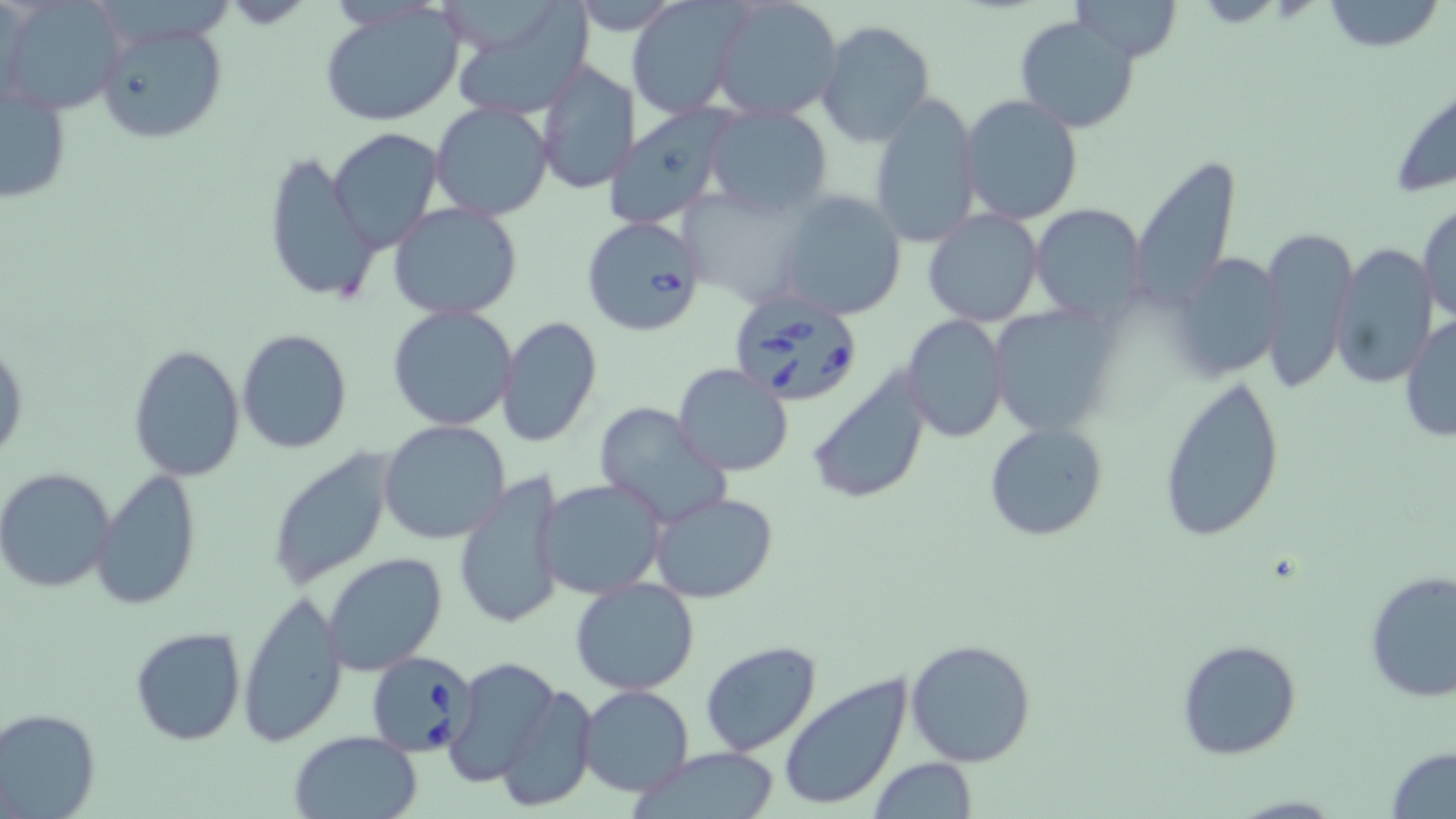

slide-level diagnosis = Babesia divergens
preparation = thin blood film
stain = May-Grünwald-Giemsa
image size = 1456×819 pixels
field of view = one of a larger specimen
magnification = 1000x
Babesia divergens-infected red blood cell locations = approximate bounding boxes as (x1, y1, x2, y2) in pixels: (580, 215, 709, 339), (729, 291, 863, 408), (367, 651, 480, 757)
modality = optical microscopy
uninfected red blood cell locations = approximate bounding boxes as (x1, y1, x2, y2) in pixels: (2, 0, 125, 116), (626, 0, 743, 120), (710, 0, 845, 122), (1071, 0, 1181, 62), (1320, 0, 1442, 52), (446, 2, 595, 120), (318, 4, 465, 127), (1015, 14, 1142, 132), (95, 17, 230, 148), (816, 20, 936, 146), (535, 61, 639, 196), (1, 74, 73, 207), (1385, 79, 1456, 199), (867, 94, 981, 248), (957, 94, 1084, 227), (430, 101, 555, 221), (605, 104, 733, 229), (703, 105, 834, 218), (327, 128, 444, 255), (263, 149, 376, 305), (1126, 155, 1244, 315), (777, 190, 907, 317), (1416, 200, 1455, 329), (390, 201, 523, 319), (1029, 203, 1147, 324), (923, 208, 1043, 327), (1254, 223, 1358, 396), (1330, 243, 1438, 390), (1168, 253, 1286, 380), (982, 303, 1119, 437), (387, 304, 518, 431), (903, 315, 1008, 442), (1399, 315, 1456, 443), (496, 317, 602, 449), (236, 328, 353, 454), (0, 335, 29, 473), (128, 343, 245, 481), (672, 363, 794, 477), (806, 366, 932, 506), (1156, 374, 1285, 544), (593, 402, 729, 529), (377, 419, 511, 545), (984, 421, 1109, 543), (265, 450, 394, 589), (90, 467, 203, 612), (0, 468, 119, 595), (454, 471, 568, 631), (537, 479, 667, 600), (650, 490, 779, 604), (323, 553, 449, 677), (1363, 570, 1456, 703), (571, 577, 698, 695), (236, 591, 347, 747), (129, 627, 246, 746), (905, 638, 1037, 767), (1175, 638, 1301, 760), (698, 641, 821, 756), (443, 657, 563, 788), (777, 673, 914, 812), (498, 681, 597, 808), (577, 685, 695, 797), (0, 707, 101, 819), (288, 731, 424, 819), (1386, 746, 1456, 819), (635, 748, 783, 819), (868, 758, 979, 817)